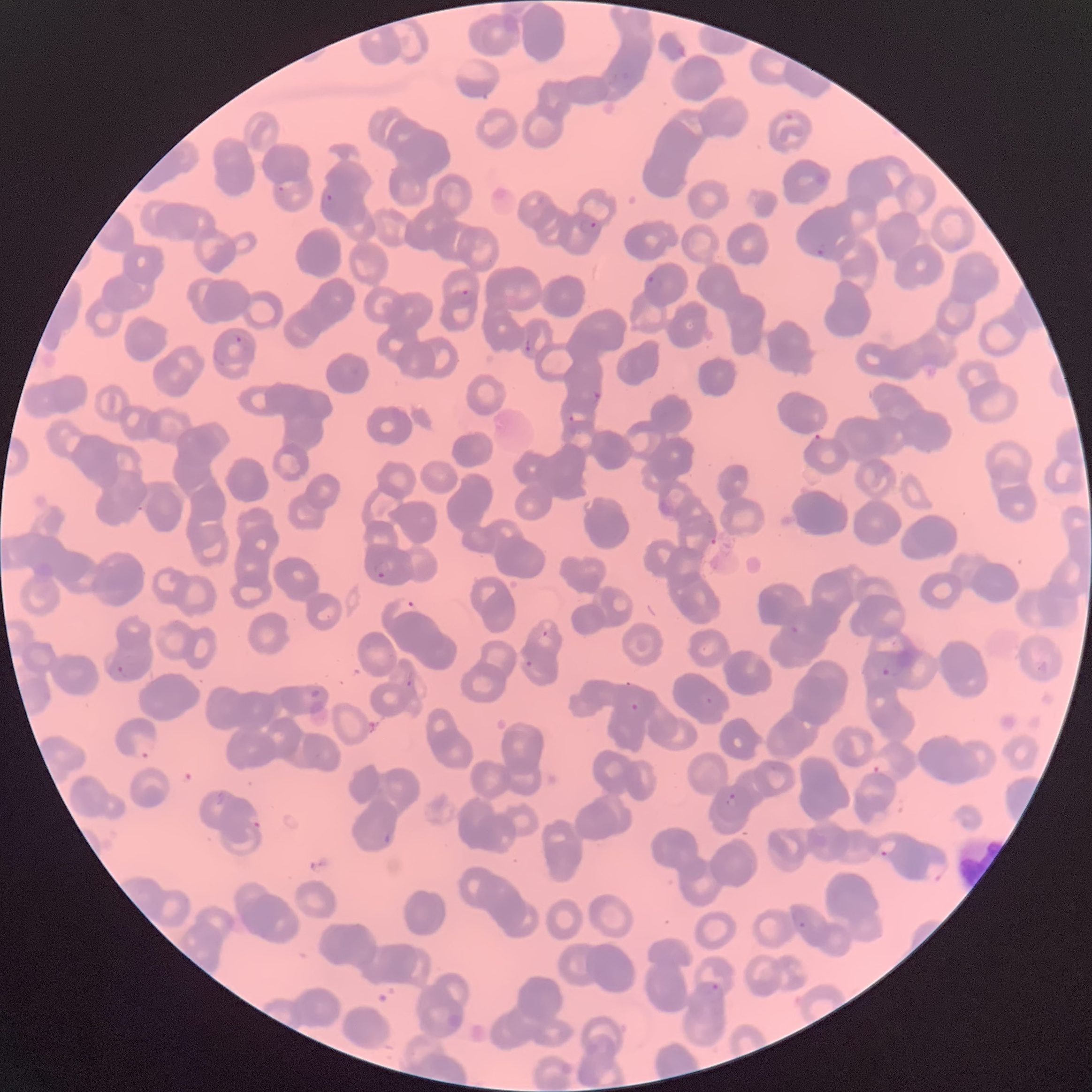
Approximate bounding boxes as (x1, y1, x2, y2) in pixels. Plasmodium parasite locations: (785, 111, 794, 121), (276, 185, 285, 193), (322, 193, 336, 204), (580, 217, 599, 234), (817, 238, 827, 255), (647, 273, 662, 290), (456, 289, 477, 304), (228, 332, 243, 346), (525, 338, 533, 352), (593, 391, 602, 404), (569, 410, 588, 424), (372, 559, 394, 579), (392, 599, 421, 619), (790, 625, 800, 634), (542, 629, 549, 638), (525, 660, 533, 668), (881, 660, 905, 678), (116, 663, 132, 677), (407, 671, 415, 690), (706, 696, 715, 705), (629, 702, 639, 711), (134, 735, 155, 757), (725, 794, 738, 807), (250, 815, 261, 831), (383, 830, 393, 844), (876, 835, 897, 860), (794, 910, 810, 929), (705, 980, 724, 1007). Thin blood film. Optical microscopy. Image is 1092×1092 pixels. The red blood cells show rouleaux formation.